Classify this cell by malaria status.
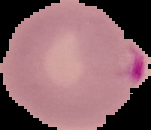

It is parasitized.

preparation = thin blood film
image size = 151×130 pixels
image type = segmented cell region with the area outside set to black